Report the malaria status of this cell.
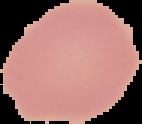

Uninfected.

From a thin blood smear. Image is 142×124 pixels. The area outside the segmented cell region is set to black.